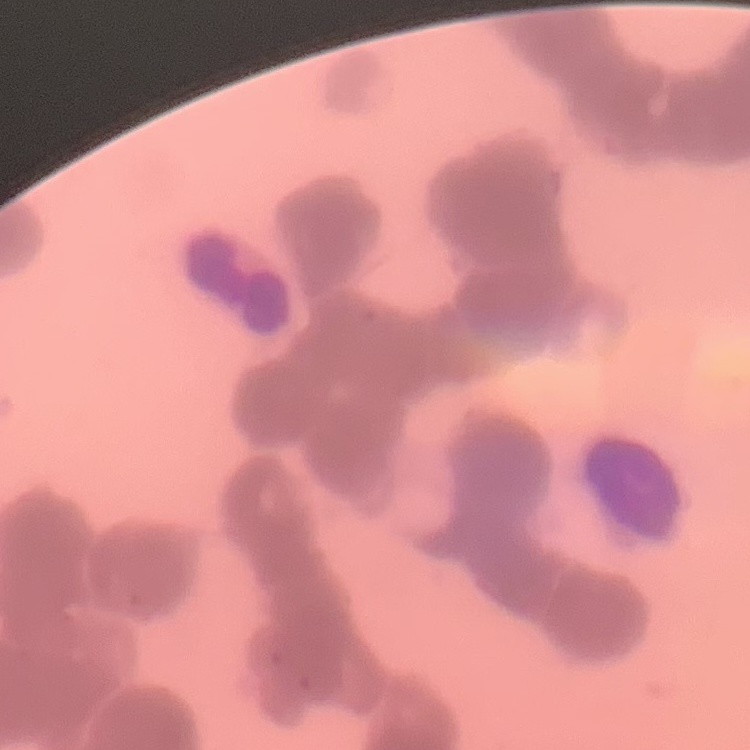
{
  "erythrocyte_morphology": "rouleaux formation",
  "image_type": "one tile cut from a larger photomicrograph",
  "stain": "Field's or Giemsa",
  "preparation": "thin peripheral smear"
}